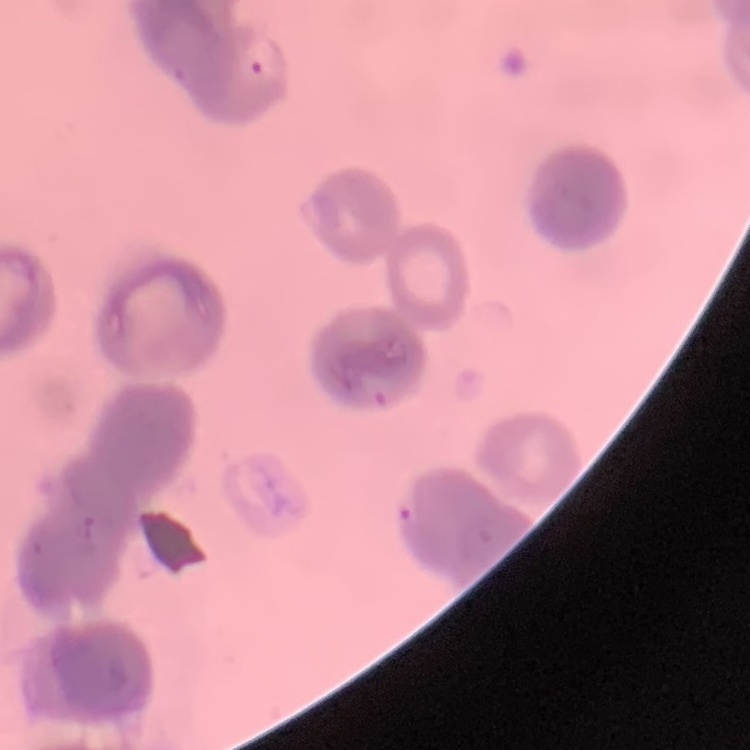
red blood cell morphology = rouleaux formation
stain = Field's or Giemsa
preparation = thin blood film
image type = square crop of a larger photomicrograph